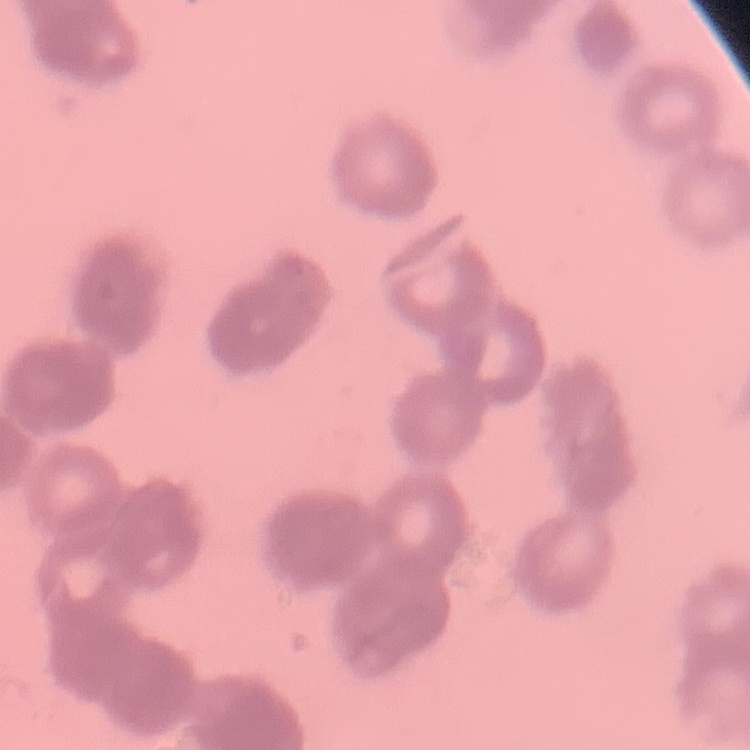

Summary:
  - Red blood cell morphology: rouleaux formation
  - Stain: Field's or Giemsa
  - Image type: one tile cut from a larger photomicrograph
  - Preparation: thin blood smear